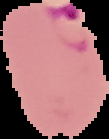

Summary:
  - Malaria status: parasitized
  - Image type: cell region segmented out of the field of view; surrounding area masked to black
  - Preparation: thin blood film
  - Image size: 109×139 pixels